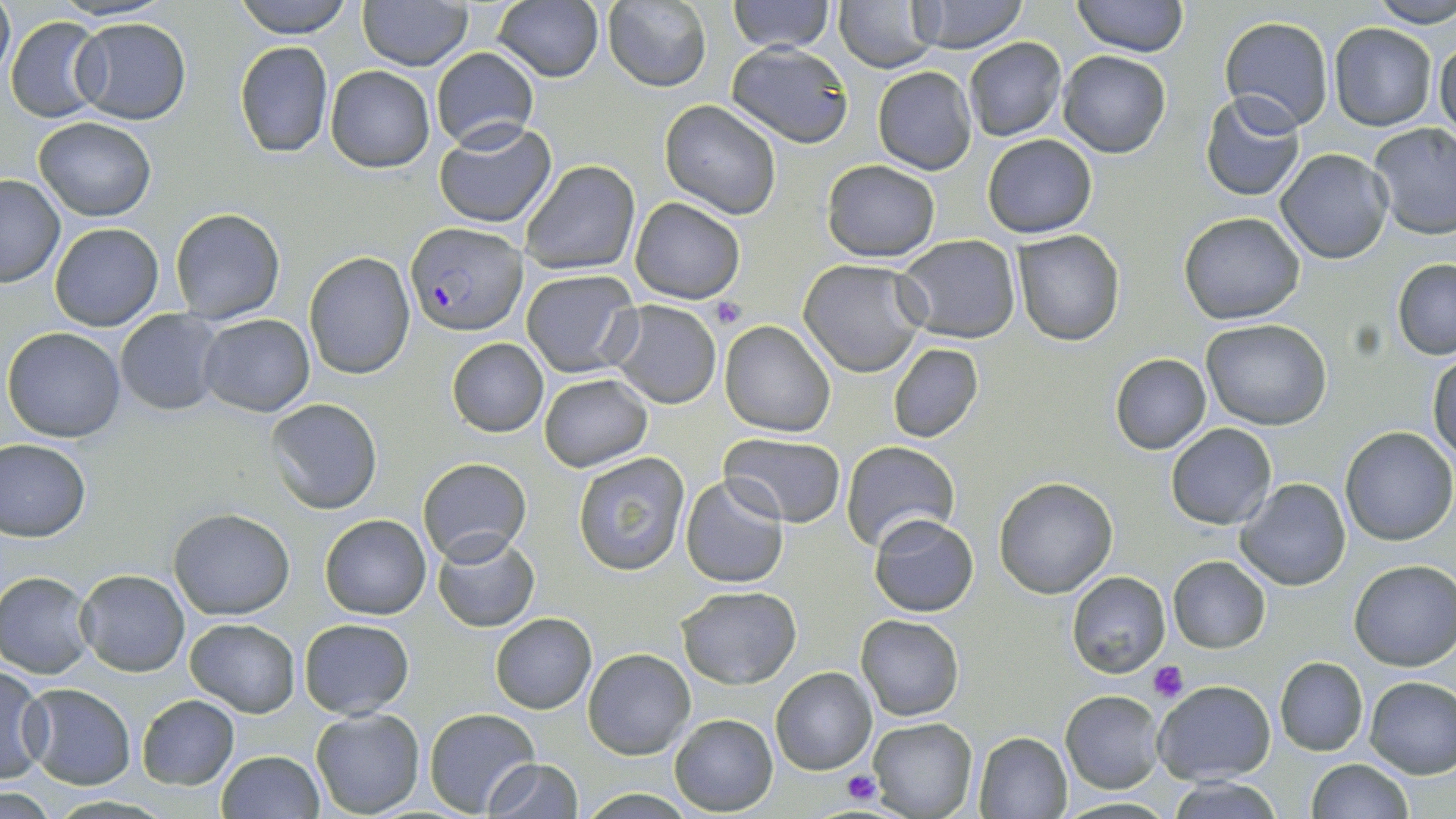
slide-level diagnosis = Plasmodium falciparum
field of view = single
preparation = thin blood film
Plasmodium falciparum-infected red blood cell locations = approximate bounding boxes as [x1, y1, x2, y2] in pixels: [405, 223, 526, 336]
modality = optical microscopy
image size = 1456×819 pixels
magnification = 1000x
stain = May-Grünwald-Giemsa
platelet locations = approximate bounding boxes as [x1, y1, x2, y2] in pixels: [706, 298, 747, 330], [1149, 659, 1186, 702], [842, 770, 880, 806]
uninfected red blood cell locations = approximate bounding boxes as [x1, y1, x2, y2] in pixels: [0, 0, 14, 81], [231, 0, 356, 39], [727, 0, 835, 53], [833, 0, 941, 73], [910, 0, 1030, 52], [1072, 0, 1188, 56], [1370, 0, 1456, 29], [357, 1, 473, 71], [493, 1, 605, 83], [603, 1, 712, 91], [5, 15, 107, 122], [69, 17, 192, 125], [1220, 17, 1335, 135], [1329, 23, 1437, 131], [1434, 35, 1456, 140], [963, 37, 1067, 142], [233, 40, 334, 157], [728, 46, 855, 145], [431, 47, 539, 150], [1058, 50, 1172, 158], [325, 65, 434, 171], [873, 65, 977, 174], [1200, 92, 1306, 202], [659, 101, 783, 220], [33, 116, 157, 222], [434, 120, 556, 229], [1368, 122, 1456, 240], [981, 134, 1098, 238], [1276, 149, 1394, 263], [520, 159, 638, 276], [822, 160, 941, 261], [0, 176, 66, 287], [631, 198, 744, 305], [170, 207, 284, 324], [1178, 211, 1306, 324], [49, 221, 164, 331], [1011, 230, 1125, 346], [894, 237, 1021, 343], [304, 252, 415, 379], [1392, 257, 1456, 359], [799, 259, 930, 378], [522, 269, 641, 377], [609, 300, 722, 408], [114, 309, 223, 415], [198, 314, 314, 418], [1201, 319, 1332, 430], [719, 320, 836, 437], [3, 327, 128, 443], [445, 338, 549, 437], [887, 343, 983, 443], [1109, 353, 1211, 455], [1429, 355, 1456, 465], [538, 373, 652, 471], [265, 398, 383, 514], [1166, 423, 1277, 529], [1340, 426, 1456, 547], [721, 433, 846, 526], [0, 436, 92, 541], [840, 440, 960, 548], [571, 452, 690, 576], [417, 457, 532, 565], [680, 475, 788, 589], [993, 477, 1118, 598], [1236, 477, 1352, 592], [168, 508, 294, 620], [867, 512, 978, 617], [319, 513, 431, 620], [430, 531, 539, 632], [1167, 555, 1271, 652], [1349, 559, 1456, 670], [77, 569, 190, 676], [1, 571, 94, 677], [1066, 571, 1171, 678], [676, 584, 800, 689], [489, 612, 596, 713], [857, 614, 964, 722], [185, 618, 300, 716], [299, 619, 415, 719], [583, 647, 696, 758], [1274, 657, 1369, 756], [1, 664, 50, 785], [771, 666, 878, 776], [1363, 675, 1456, 778], [1152, 680, 1275, 785], [24, 685, 136, 788], [1059, 691, 1163, 793], [136, 694, 240, 790], [311, 707, 426, 817], [423, 707, 539, 816], [669, 713, 777, 815], [868, 718, 977, 818], [972, 731, 1073, 818], [215, 750, 324, 819], [483, 758, 583, 818], [1307, 759, 1413, 818], [1169, 778, 1284, 818]